Report the malaria status of this cell.
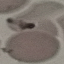
Uninfected.

image type = cell patch, automatically extracted from a larger field of view and resized to 64 × 64 pixels
preparation = thin blood smear
stain = Giemsa
capture = smartphone camera at the microscope eyepiece